Classify this cell by malaria status.
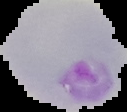

It is parasitized.

{
  "preparation": "thin blood smear",
  "image_type": "cell region segmented out of the field of view; surrounding area masked to black",
  "image_size": "127×112 pixels"
}